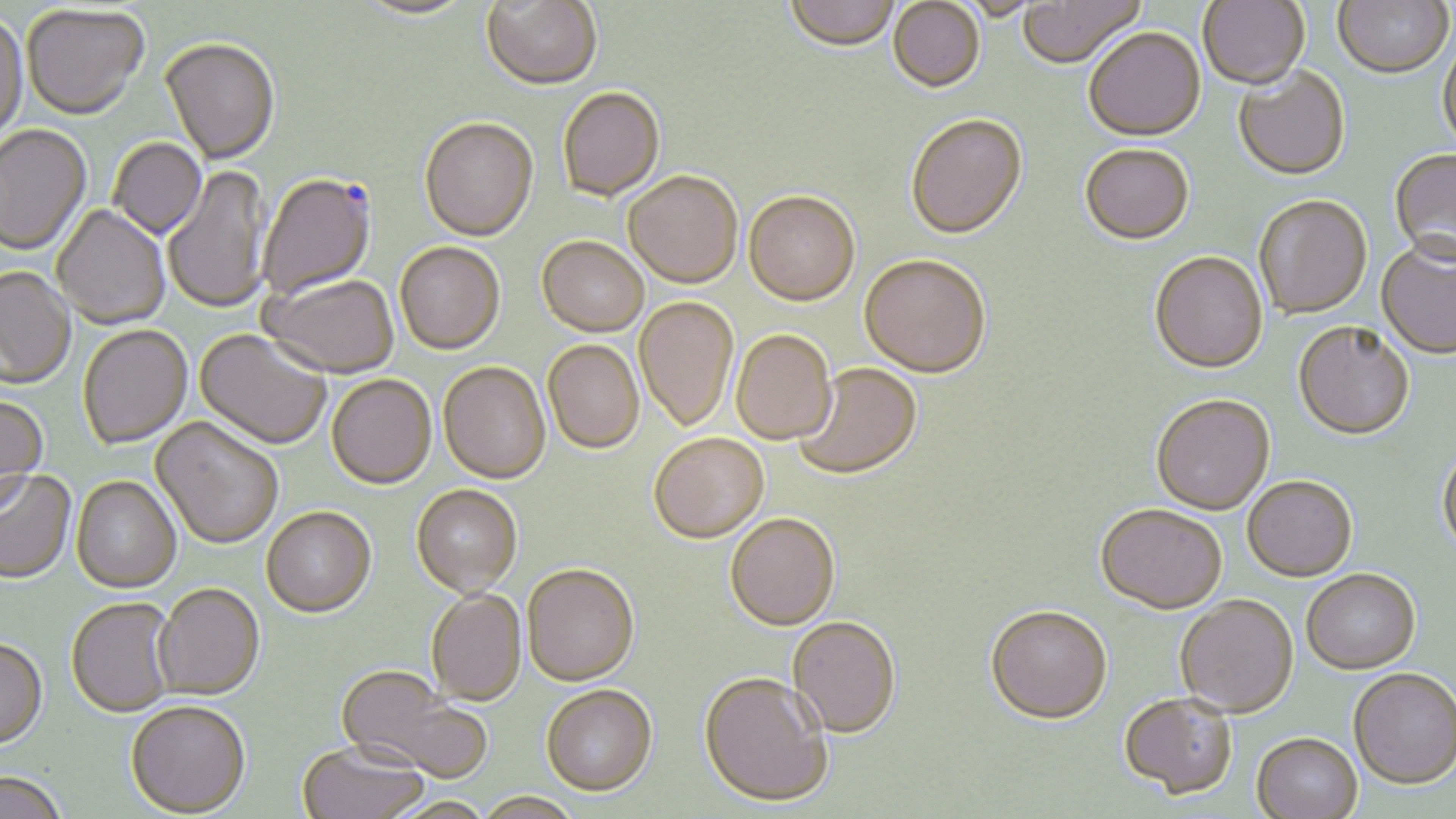

Summary:
  - Coordinate format: approximate bounding boxes as [x1, y1, x2, y2] in pixels
  - Uninfected red blood cell locations: [481, 0, 603, 92], [784, 0, 900, 54], [1017, 0, 1145, 71], [1198, 0, 1309, 90], [1333, 0, 1454, 79], [355, 1, 477, 22], [888, 1, 985, 95], [22, 6, 149, 123], [0, 14, 29, 149], [1084, 28, 1205, 143], [1437, 34, 1456, 155], [159, 40, 280, 167], [1233, 66, 1351, 181], [558, 89, 665, 203], [905, 115, 1028, 241], [419, 120, 539, 244], [0, 125, 93, 257], [108, 139, 207, 241], [1079, 144, 1194, 245], [1389, 149, 1456, 265], [163, 165, 271, 316], [623, 174, 742, 290], [743, 192, 860, 308], [1253, 195, 1372, 320], [51, 205, 171, 331], [536, 238, 648, 339], [394, 243, 505, 357], [1376, 243, 1456, 359], [1149, 251, 1268, 374], [859, 255, 991, 379], [0, 268, 77, 390], [260, 276, 399, 381], [634, 298, 738, 434], [1293, 321, 1415, 441], [78, 326, 193, 451], [731, 330, 836, 447], [194, 331, 331, 452], [543, 341, 644, 456], [793, 363, 923, 482], [438, 364, 551, 486], [327, 376, 437, 491], [1150, 394, 1275, 515], [0, 397, 49, 512], [150, 418, 284, 552], [649, 435, 769, 545], [1437, 447, 1456, 557], [0, 471, 78, 587], [1243, 475, 1357, 581], [71, 477, 182, 595], [411, 487, 523, 600], [1095, 503, 1227, 613], [262, 509, 377, 621], [724, 515, 840, 632], [522, 566, 639, 688], [1302, 570, 1421, 674], [153, 586, 265, 703], [425, 590, 527, 708], [1175, 595, 1298, 717], [66, 599, 176, 719], [985, 604, 1113, 725], [788, 616, 901, 738], [0, 641, 49, 753], [1348, 668, 1456, 791], [335, 669, 487, 783], [699, 672, 833, 808], [541, 687, 657, 798], [1118, 692, 1238, 798], [125, 704, 250, 818], [1251, 733, 1362, 818], [296, 743, 428, 819], [0, 775, 65, 819], [472, 794, 584, 819]
  - Plasmodium falciparum-infected red blood cell locations: [257, 173, 377, 300]
  - Slide-level diagnosis: Plasmodium falciparum
  - Modality: optical microscopy
  - Image size: 1456×819 pixels
  - Magnification: 1000x
  - Preparation: thin blood film
  - Stain: May-Grünwald-Giemsa
  - Field of view: one of a larger specimen